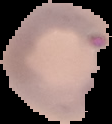

The area outside the segmented cell region is set to black. From a thin blood smear. Image is 112×124 pixels. Malaria status: parasitized.